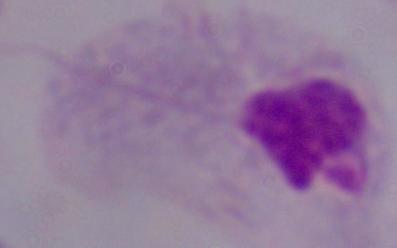

Summary:
  - Modality: photomicrograph
  - Identification: trichomonad
  - Magnification: 1000x